Assess the morphology of the erythrocytes.
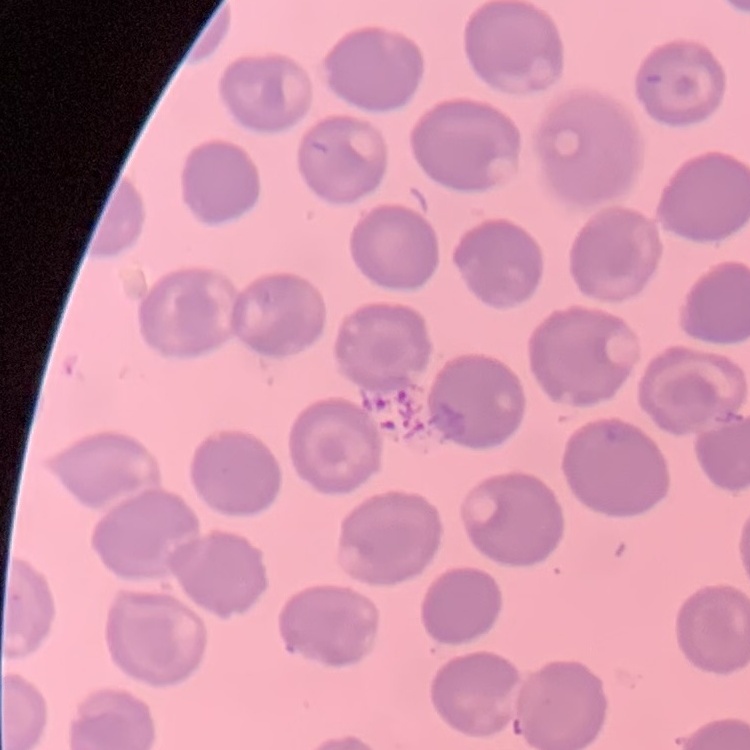
They show no rouleaux formation.

Field's or Giemsa stain. Square crop of a larger photomicrograph. Thin peripheral smear.